Name the cell type shown.
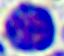
This is a leukocyte.

Photomicrograph. Captured at 400x magnification.